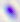
magnification = 400x
modality = photomicrograph
identification = Toxoplasma gondii